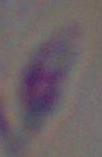

Summary:
  - Identification: Toxoplasma gondii
  - Magnification: 1000x
  - Modality: photomicrograph